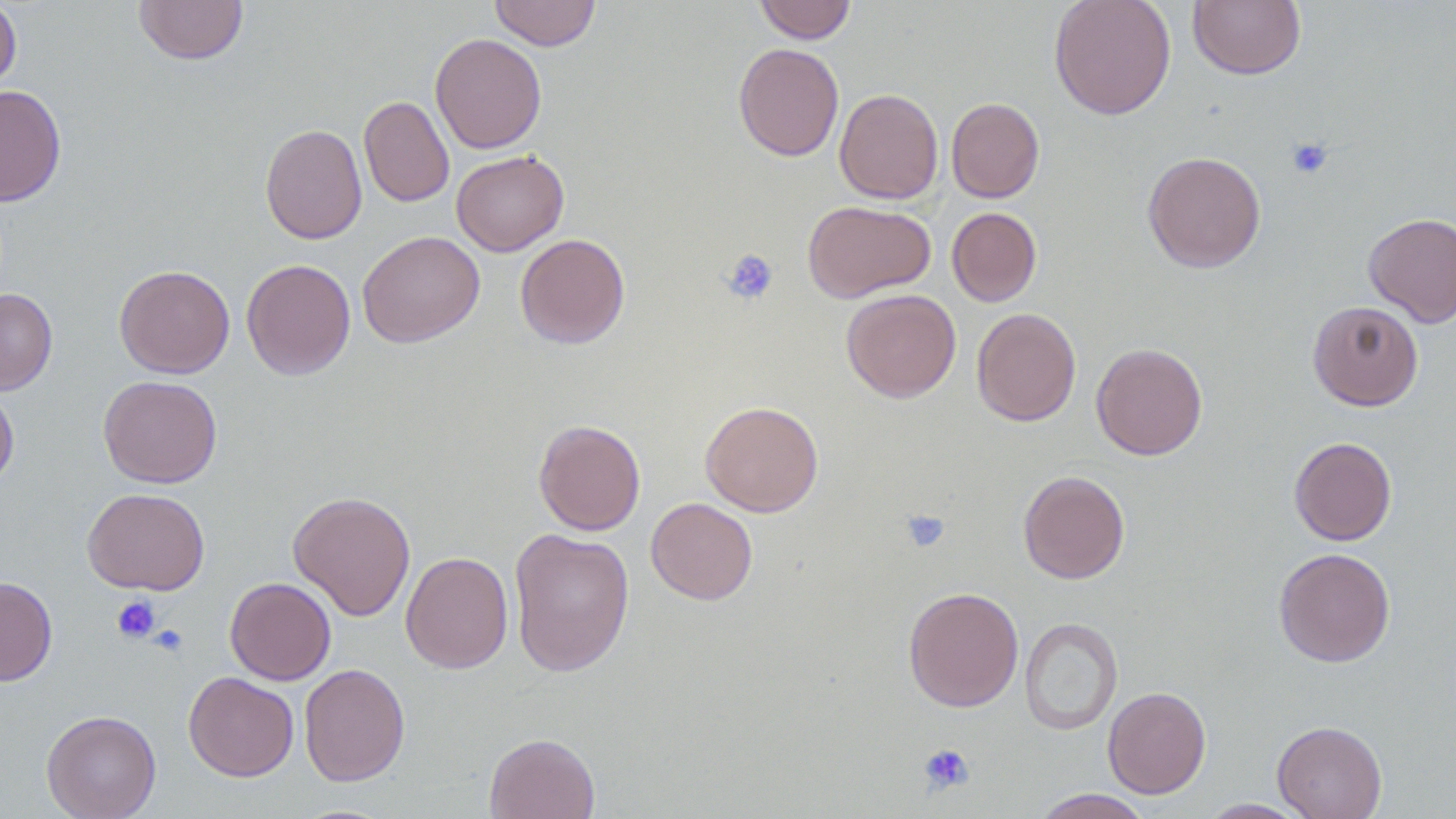
Summary:
  - Coordinate format: approximate bounding boxes as (x1, y1, x2, y2) in pixels
  - Uninfected red blood cell locations: (0, 0, 21, 97), (134, 0, 249, 65), (489, 0, 601, 51), (754, 0, 857, 43), (1048, 0, 1177, 120), (1188, 0, 1306, 80), (430, 33, 547, 153), (733, 43, 844, 161), (0, 85, 67, 207), (834, 87, 943, 205), (359, 96, 454, 208), (946, 97, 1045, 202), (260, 123, 367, 244), (451, 150, 569, 256), (1142, 151, 1266, 273), (803, 200, 936, 302), (946, 206, 1041, 307), (1363, 211, 1456, 327), (515, 233, 630, 349), (362, 234, 488, 351), (241, 258, 356, 381), (114, 264, 235, 378), (0, 288, 58, 395), (841, 288, 961, 403), (1307, 300, 1424, 411), (971, 307, 1081, 426), (1091, 342, 1208, 460), (98, 375, 222, 488), (0, 385, 19, 492), (700, 400, 823, 517), (534, 419, 646, 536), (1289, 436, 1397, 546), (1018, 470, 1130, 584), (82, 487, 210, 595), (288, 490, 416, 621), (645, 497, 759, 605), (508, 528, 635, 677), (1274, 547, 1396, 667), (400, 551, 514, 674), (0, 576, 57, 686), (225, 577, 336, 685), (903, 586, 1023, 712), (1020, 616, 1123, 735), (299, 662, 410, 786), (183, 672, 299, 782), (1103, 686, 1211, 799), (41, 709, 161, 819), (1272, 720, 1387, 819), (484, 732, 600, 819), (1032, 788, 1153, 818), (1198, 799, 1312, 818)
  - Platelet locations: (1287, 137, 1334, 179), (720, 249, 779, 305), (900, 508, 951, 553), (111, 595, 161, 643), (149, 623, 188, 657), (918, 742, 974, 795)
  - Slide-level diagnosis: negative for blood parasites
  - Modality: light microscopy
  - Image size: 1456×819 pixels
  - Field of view: one of a larger specimen
  - Magnification: 1000x
  - Preparation: thin blood film